Outline each blood parasite and name the species.
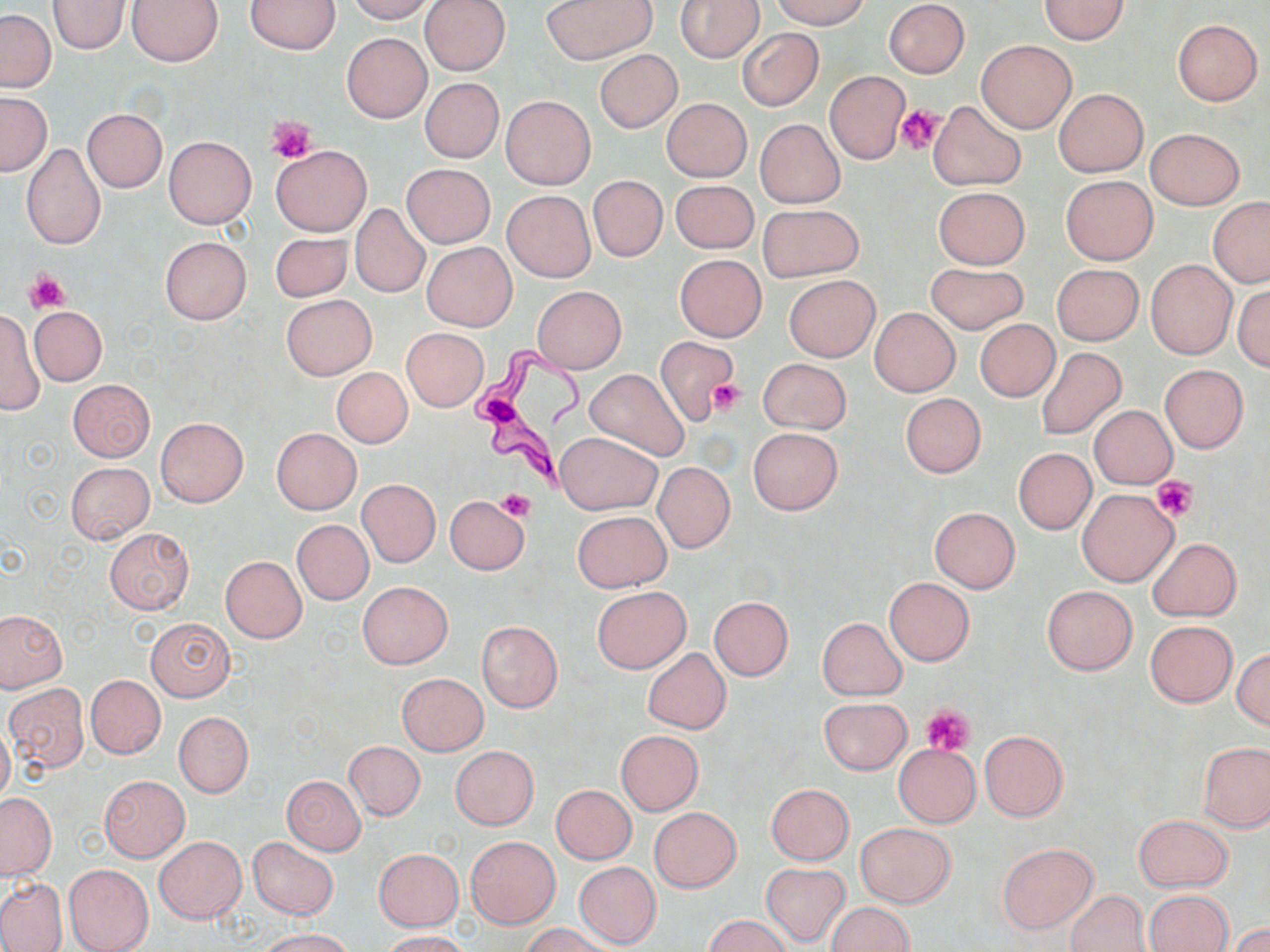
Approximate bounding boxes as (x1, y1, x2, y2) in pixels.
Trypanosoma brucei: (470, 342, 591, 496).
No Plasmodium falciparum, Plasmodium ovale, Plasmodium malariae, Plasmodium vivax, or Babesia divergens observed.

Summary:
  - Platelet locations: (896, 105, 944, 158), (265, 116, 316, 164), (27, 272, 69, 312), (707, 379, 746, 416), (1152, 476, 1197, 521), (499, 488, 535, 521), (922, 703, 975, 756)
  - Uninfected red blood cell locations: (127, 0, 224, 66), (344, 0, 437, 23), (421, 0, 510, 75), (541, 0, 654, 65), (674, 0, 764, 63), (772, 0, 869, 28), (883, 0, 969, 78), (1039, 0, 1130, 43), (48, 1, 130, 54), (247, 1, 341, 53), (0, 10, 56, 92), (1172, 20, 1262, 105), (737, 28, 823, 110), (341, 33, 432, 123), (977, 39, 1075, 133), (595, 49, 682, 132), (824, 70, 909, 164), (419, 77, 503, 162), (1055, 88, 1147, 177), (1, 91, 51, 175), (500, 96, 596, 190), (662, 98, 751, 182), (928, 101, 1025, 192), (81, 109, 167, 192), (754, 118, 845, 208), (1146, 128, 1244, 209), (164, 136, 256, 229), (21, 142, 106, 251), (271, 144, 372, 236), (402, 164, 495, 248), (1061, 175, 1158, 265), (588, 176, 667, 262), (670, 180, 758, 253), (933, 186, 1031, 269), (502, 190, 596, 282), (1208, 198, 1270, 287), (350, 204, 429, 297), (760, 204, 861, 281), (270, 232, 353, 302), (159, 235, 252, 324), (421, 242, 518, 332), (675, 255, 766, 341), (1146, 259, 1238, 360), (925, 262, 1027, 334), (1051, 263, 1143, 345), (785, 275, 879, 361), (1233, 283, 1270, 372), (531, 286, 627, 373), (281, 295, 377, 379), (0, 305, 43, 416), (30, 307, 106, 385), (870, 308, 960, 396), (975, 320, 1060, 401), (402, 328, 488, 411), (655, 336, 738, 425), (1036, 347, 1126, 440), (758, 358, 851, 434), (1160, 365, 1248, 452), (331, 368, 412, 448), (584, 368, 690, 461), (67, 379, 154, 461), (899, 392, 986, 478), (1089, 405, 1177, 488), (156, 417, 248, 507), (271, 427, 362, 515), (748, 428, 842, 515), (555, 432, 660, 514), (1013, 448, 1096, 534), (66, 462, 154, 543), (653, 462, 735, 552), (357, 479, 441, 567), (1077, 489, 1178, 586), (445, 495, 528, 575), (929, 507, 1020, 592), (574, 511, 670, 593), (292, 520, 373, 605), (103, 528, 193, 614), (1149, 538, 1242, 621), (220, 556, 306, 643), (885, 577, 974, 665), (358, 581, 452, 668), (1042, 585, 1136, 674), (592, 587, 690, 673), (709, 597, 793, 680), (0, 611, 66, 691), (145, 617, 237, 702), (818, 617, 906, 699), (1145, 621, 1237, 707), (477, 622, 563, 711), (642, 648, 731, 734), (1232, 649, 1270, 729), (398, 673, 488, 755), (86, 675, 165, 758), (5, 684, 90, 772), (819, 697, 911, 774), (174, 711, 254, 797), (0, 721, 14, 805), (616, 730, 703, 815), (979, 730, 1068, 821), (345, 741, 425, 821), (1198, 741, 1270, 832), (893, 743, 982, 827), (451, 746, 538, 829), (100, 775, 190, 862), (283, 776, 365, 855), (766, 784, 854, 864), (551, 785, 636, 864), (0, 793, 56, 879), (648, 807, 742, 893), (1133, 814, 1232, 892), (855, 822, 956, 907), (155, 836, 246, 923), (466, 836, 559, 928), (248, 837, 338, 918), (998, 842, 1099, 934), (373, 849, 463, 931), (573, 861, 662, 949), (760, 863, 851, 946), (64, 864, 154, 952), (0, 877, 67, 951), (1064, 889, 1151, 952), (1146, 890, 1233, 952), (825, 902, 913, 952), (705, 914, 791, 952), (1229, 923, 1270, 952), (522, 924, 615, 952), (259, 928, 356, 952), (378, 930, 470, 952)
  - Slide-level diagnosis: Trypanosoma brucei
  - Preparation: thin blood smear
  - Field of view: one of a larger specimen
  - Image size: 1270×952 pixels
  - Stain: May-Grünwald-Giemsa
  - Modality: optical microscopy
  - Magnification: 1000x